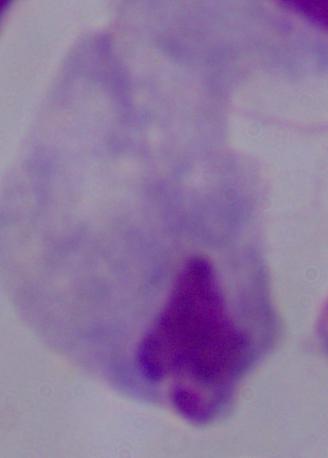

magnification = 1000x
identification = trichomonad
modality = photomicrograph